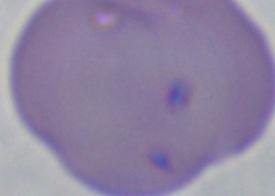
Captured at 1000x magnification. A Babesia parasite is shown. Photomicrograph.